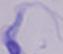

A trypanosome is seen. Micrograph. 1000x magnification.